Give the position of every malaria parasite.
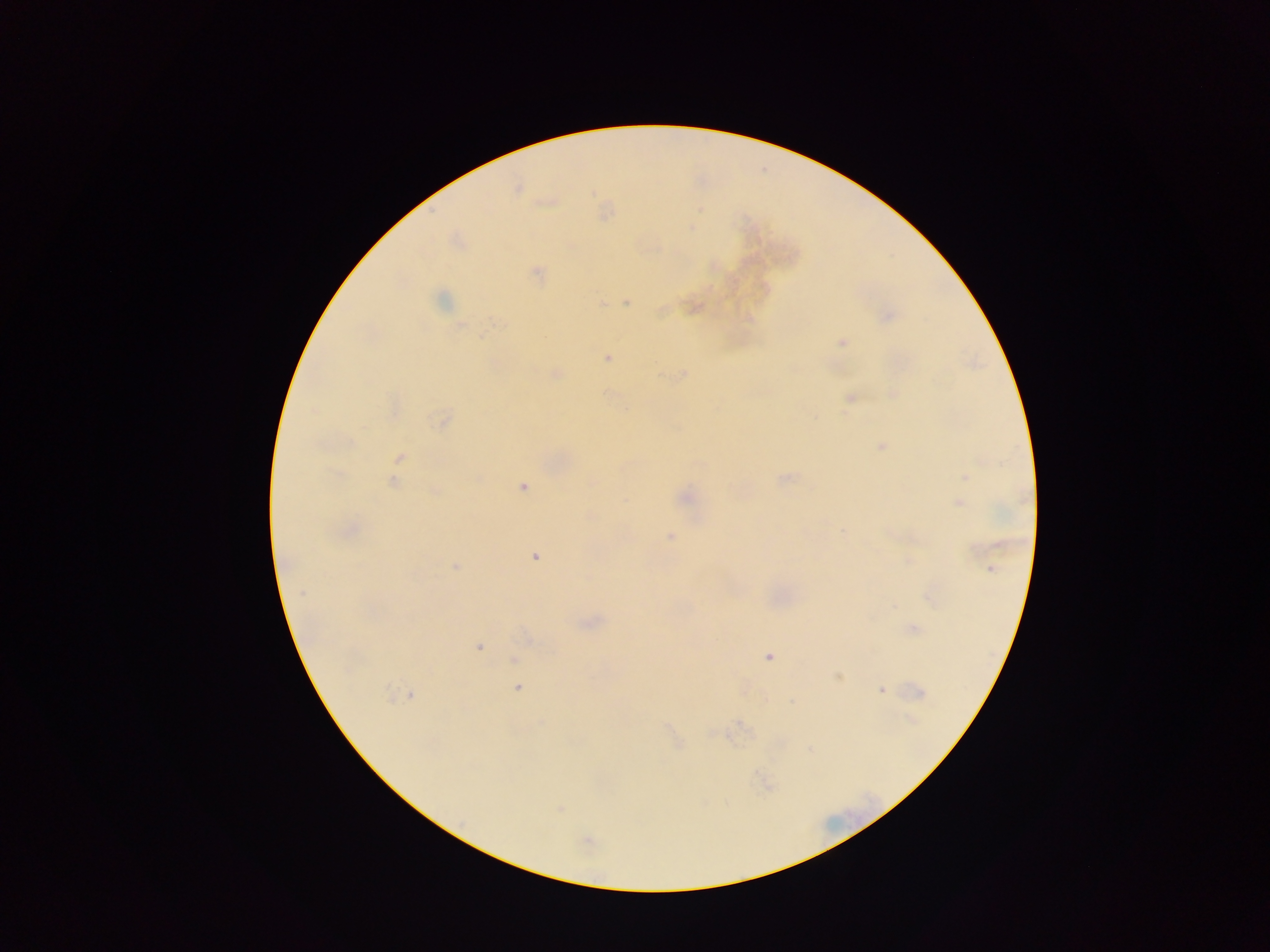
Approximate centers as (x, y) in pixels.
Malaria parasites: (517, 189), (537, 272), (441, 300), (627, 302), (603, 303), (886, 316), (748, 318), (461, 326), (842, 342), (606, 357), (556, 373), (684, 374), (851, 398), (814, 417), (443, 420), (350, 443), (882, 446), (400, 458), (964, 476), (784, 478), (393, 482), (522, 487), (435, 491), (685, 497), (959, 503), (590, 516), (350, 530), (843, 532), (670, 537), (535, 556), (455, 566), (991, 569), (302, 593), (914, 629), (479, 647), (768, 657), (514, 659), (838, 676), (518, 687), (881, 690), (922, 692), (389, 693), (410, 695), (910, 720), (542, 723), (559, 809), (587, 841).

Summary:
  - Capture: mobile-phone photograph through a microscope
  - Field of view: single
  - Image size: 1270×952 pixels
  - Preparation: thick blood smear
  - Country: Ghana